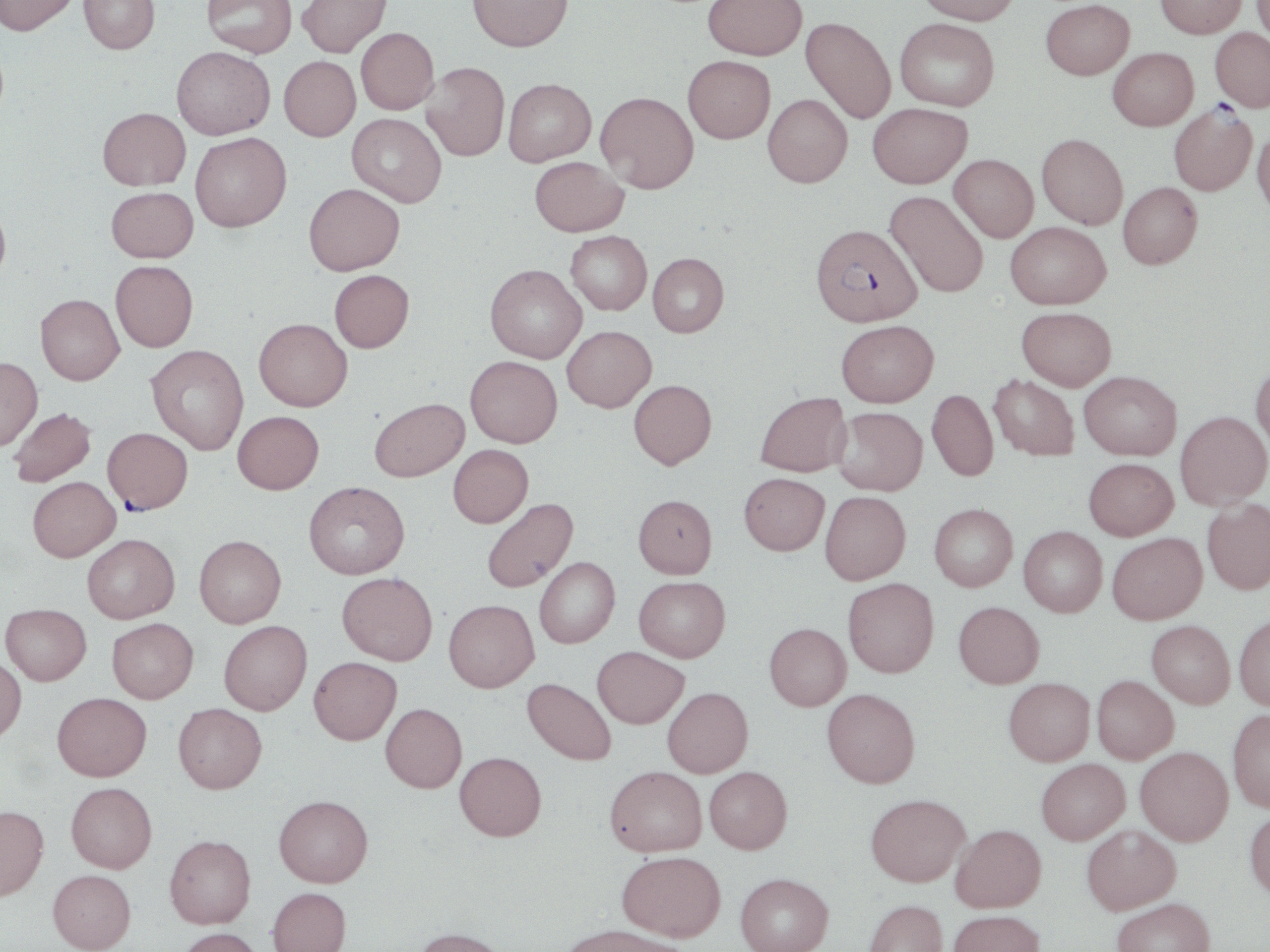 Approximate bounding boxes as named x1/y1/x2/y2 corners in pixels. Plasmodium falciparum-infected red blood cell locations: (x1=1168, y1=103, x2=1257, y2=196), (x1=811, y1=223, x2=922, y2=326), (x1=103, y1=428, x2=192, y2=514). Uninfected red blood cell locations: (x1=0, y1=0, x2=80, y2=36), (x1=79, y1=0, x2=160, y2=53), (x1=202, y1=0, x2=296, y2=58), (x1=297, y1=0, x2=391, y2=57), (x1=467, y1=0, x2=573, y2=51), (x1=703, y1=0, x2=808, y2=59), (x1=916, y1=0, x2=1020, y2=24), (x1=1155, y1=0, x2=1246, y2=38), (x1=1251, y1=0, x2=1270, y2=48), (x1=1041, y1=1, x2=1134, y2=80), (x1=801, y1=16, x2=896, y2=124), (x1=895, y1=18, x2=999, y2=110), (x1=356, y1=27, x2=439, y2=114), (x1=1211, y1=28, x2=1270, y2=112), (x1=172, y1=46, x2=275, y2=139), (x1=1108, y1=47, x2=1197, y2=130), (x1=683, y1=55, x2=775, y2=143), (x1=279, y1=56, x2=361, y2=141), (x1=421, y1=62, x2=510, y2=161), (x1=503, y1=78, x2=596, y2=166), (x1=595, y1=91, x2=698, y2=193), (x1=763, y1=94, x2=852, y2=187), (x1=868, y1=102, x2=971, y2=188), (x1=97, y1=107, x2=190, y2=190), (x1=347, y1=113, x2=446, y2=207), (x1=1252, y1=126, x2=1270, y2=219), (x1=190, y1=132, x2=291, y2=232), (x1=1037, y1=133, x2=1128, y2=229), (x1=949, y1=154, x2=1038, y2=242), (x1=530, y1=156, x2=628, y2=236), (x1=1118, y1=181, x2=1203, y2=269), (x1=304, y1=183, x2=404, y2=275), (x1=106, y1=187, x2=198, y2=263), (x1=884, y1=190, x2=989, y2=297), (x1=0, y1=199, x2=11, y2=286), (x1=1004, y1=221, x2=1111, y2=309), (x1=566, y1=230, x2=652, y2=315), (x1=647, y1=252, x2=728, y2=337), (x1=110, y1=260, x2=198, y2=350), (x1=485, y1=263, x2=586, y2=363), (x1=329, y1=269, x2=414, y2=352), (x1=35, y1=294, x2=124, y2=384), (x1=1016, y1=306, x2=1117, y2=390), (x1=254, y1=318, x2=352, y2=411), (x1=836, y1=319, x2=938, y2=406), (x1=562, y1=325, x2=656, y2=412), (x1=146, y1=344, x2=249, y2=455), (x1=465, y1=356, x2=562, y2=447), (x1=0, y1=357, x2=42, y2=450), (x1=1250, y1=358, x2=1270, y2=454), (x1=1079, y1=370, x2=1181, y2=459), (x1=988, y1=374, x2=1079, y2=461), (x1=628, y1=379, x2=717, y2=469), (x1=927, y1=389, x2=998, y2=481), (x1=755, y1=391, x2=851, y2=477), (x1=369, y1=397, x2=469, y2=482), (x1=833, y1=406, x2=927, y2=495), (x1=8, y1=407, x2=96, y2=487), (x1=232, y1=411, x2=324, y2=494), (x1=1175, y1=411, x2=1269, y2=510), (x1=448, y1=444, x2=533, y2=527), (x1=1083, y1=457, x2=1178, y2=540), (x1=739, y1=473, x2=829, y2=555), (x1=28, y1=477, x2=121, y2=561), (x1=304, y1=481, x2=409, y2=579), (x1=820, y1=491, x2=910, y2=584), (x1=633, y1=494, x2=717, y2=578), (x1=482, y1=497, x2=578, y2=593), (x1=1202, y1=498, x2=1270, y2=594), (x1=929, y1=503, x2=1017, y2=591), (x1=1019, y1=526, x2=1107, y2=617), (x1=1107, y1=532, x2=1207, y2=624), (x1=82, y1=534, x2=179, y2=623), (x1=194, y1=535, x2=286, y2=627), (x1=534, y1=557, x2=620, y2=648), (x1=337, y1=572, x2=438, y2=665), (x1=634, y1=576, x2=730, y2=661), (x1=843, y1=578, x2=939, y2=677), (x1=444, y1=599, x2=539, y2=692), (x1=954, y1=601, x2=1044, y2=688), (x1=1, y1=603, x2=91, y2=685), (x1=1234, y1=614, x2=1270, y2=710), (x1=107, y1=618, x2=198, y2=703), (x1=219, y1=620, x2=311, y2=715), (x1=1147, y1=620, x2=1235, y2=708), (x1=764, y1=623, x2=851, y2=710), (x1=593, y1=647, x2=689, y2=728), (x1=0, y1=656, x2=26, y2=742), (x1=309, y1=657, x2=401, y2=744), (x1=1092, y1=675, x2=1178, y2=763), (x1=1004, y1=677, x2=1095, y2=765), (x1=522, y1=678, x2=616, y2=765), (x1=663, y1=687, x2=753, y2=777), (x1=822, y1=688, x2=920, y2=788), (x1=52, y1=692, x2=151, y2=781), (x1=173, y1=703, x2=267, y2=793), (x1=380, y1=703, x2=467, y2=792), (x1=1228, y1=708, x2=1270, y2=812), (x1=1135, y1=746, x2=1233, y2=845), (x1=455, y1=751, x2=546, y2=840), (x1=1036, y1=758, x2=1129, y2=845), (x1=605, y1=765, x2=707, y2=856), (x1=704, y1=766, x2=792, y2=853), (x1=66, y1=782, x2=157, y2=873), (x1=865, y1=793, x2=970, y2=886), (x1=274, y1=794, x2=373, y2=887), (x1=0, y1=805, x2=48, y2=901), (x1=1245, y1=808, x2=1270, y2=901), (x1=950, y1=823, x2=1046, y2=912), (x1=1082, y1=824, x2=1181, y2=915), (x1=164, y1=834, x2=256, y2=929), (x1=617, y1=850, x2=727, y2=940), (x1=47, y1=869, x2=136, y2=952), (x1=735, y1=872, x2=833, y2=952), (x1=267, y1=887, x2=351, y2=952), (x1=1112, y1=897, x2=1217, y2=952), (x1=864, y1=899, x2=948, y2=952), (x1=947, y1=909, x2=1045, y2=952), (x1=558, y1=923, x2=691, y2=952), (x1=413, y1=927, x2=510, y2=952), (x1=178, y1=928, x2=263, y2=952). Slide-level diagnosis: Plasmodium falciparum. One field of a larger specimen. Captured at 1000x magnification. Thin blood film. Optical microscopy. May-Grünwald-Giemsa stain. Image is 1270×952 pixels.